Locate and identify every blood parasite.
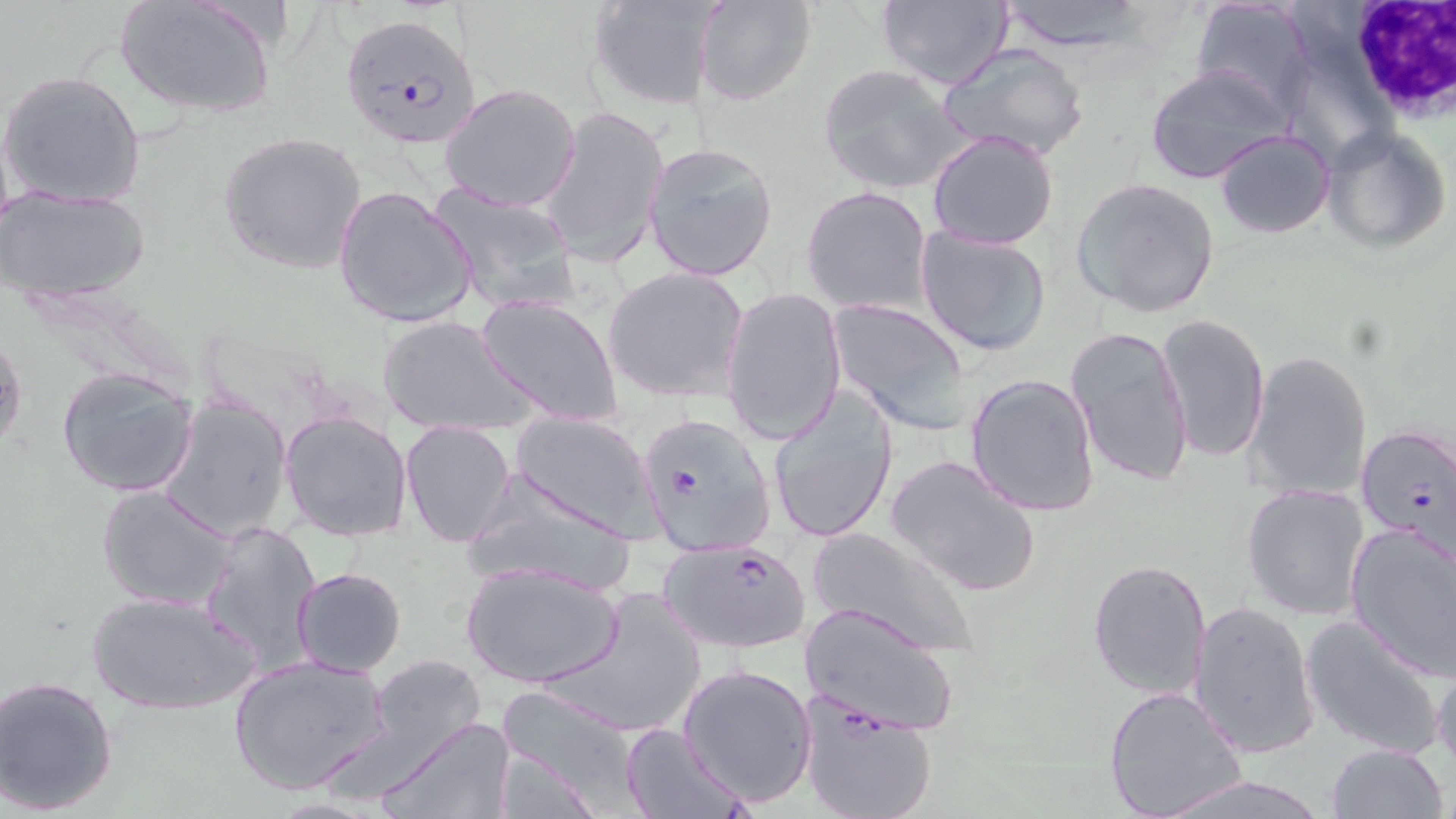

Approximate bounding boxes as named x1/y1/x2/y2 corners in pixels.
Plasmodium falciparum-infected red blood cells (subset): (x1=342, y1=12, x2=481, y2=150), (x1=639, y1=413, x2=777, y2=557), (x1=1355, y1=423, x2=1456, y2=558), (x1=654, y1=533, x2=807, y2=650), (x1=797, y1=694, x2=938, y2=819).
No Plasmodium ovale, Plasmodium malariae, Plasmodium vivax, Babesia divergens, or Trypanosoma brucei observed.

slide-level diagnosis = Plasmodium falciparum
magnification = 1000x
stain = May-Grünwald-Giemsa
field of view = single
uninfected red blood cell locations = approximate bounding boxes as named x1/y1/x2/y2 corners in pixels: (x1=115, y1=0, x2=276, y2=121), (x1=586, y1=0, x2=724, y2=110), (x1=693, y1=0, x2=817, y2=107), (x1=873, y1=0, x2=1014, y2=91), (x1=993, y1=0, x2=1155, y2=53), (x1=1189, y1=1, x2=1315, y2=115), (x1=938, y1=43, x2=1089, y2=162), (x1=1144, y1=62, x2=1293, y2=185), (x1=817, y1=64, x2=969, y2=195), (x1=1, y1=70, x2=146, y2=209), (x1=439, y1=83, x2=583, y2=213), (x1=538, y1=105, x2=668, y2=271), (x1=1321, y1=126, x2=1452, y2=254), (x1=926, y1=129, x2=1060, y2=249), (x1=1214, y1=129, x2=1335, y2=239), (x1=217, y1=131, x2=368, y2=275), (x1=644, y1=142, x2=779, y2=282), (x1=1071, y1=177, x2=1222, y2=318), (x1=331, y1=184, x2=479, y2=329), (x1=429, y1=184, x2=582, y2=316), (x1=801, y1=185, x2=932, y2=315), (x1=2, y1=188, x2=151, y2=301), (x1=915, y1=228, x2=1053, y2=357), (x1=603, y1=265, x2=751, y2=404), (x1=723, y1=286, x2=847, y2=446), (x1=476, y1=293, x2=625, y2=428), (x1=828, y1=298, x2=974, y2=433), (x1=1154, y1=313, x2=1270, y2=462), (x1=377, y1=314, x2=536, y2=438), (x1=1066, y1=326, x2=1192, y2=490), (x1=0, y1=331, x2=25, y2=453), (x1=1243, y1=348, x2=1374, y2=503), (x1=57, y1=367, x2=200, y2=498), (x1=964, y1=373, x2=1100, y2=518), (x1=768, y1=387, x2=899, y2=543), (x1=158, y1=393, x2=293, y2=543), (x1=281, y1=408, x2=414, y2=542), (x1=508, y1=411, x2=663, y2=540), (x1=400, y1=419, x2=516, y2=546), (x1=885, y1=453, x2=1042, y2=598), (x1=462, y1=471, x2=640, y2=596), (x1=1241, y1=482, x2=1371, y2=620), (x1=96, y1=485, x2=239, y2=612), (x1=197, y1=519, x2=325, y2=678), (x1=1343, y1=520, x2=1456, y2=679), (x1=807, y1=523, x2=980, y2=659), (x1=459, y1=558, x2=625, y2=689), (x1=1087, y1=559, x2=1211, y2=699), (x1=291, y1=567, x2=408, y2=678), (x1=540, y1=587, x2=709, y2=734), (x1=88, y1=591, x2=259, y2=716), (x1=1189, y1=599, x2=1319, y2=758), (x1=800, y1=602, x2=962, y2=737), (x1=1300, y1=614, x2=1449, y2=760), (x1=1430, y1=649, x2=1456, y2=775), (x1=228, y1=653, x2=393, y2=796), (x1=368, y1=655, x2=484, y2=760), (x1=678, y1=663, x2=817, y2=807), (x1=1, y1=677, x2=120, y2=815), (x1=1103, y1=685, x2=1247, y2=819), (x1=495, y1=691, x2=639, y2=813), (x1=379, y1=716, x2=518, y2=819), (x1=619, y1=720, x2=748, y2=819), (x1=1325, y1=743, x2=1450, y2=819), (x1=1158, y1=772, x2=1337, y2=819)
image size = 1456×819 pixels
modality = light microscopy
preparation = thin blood film